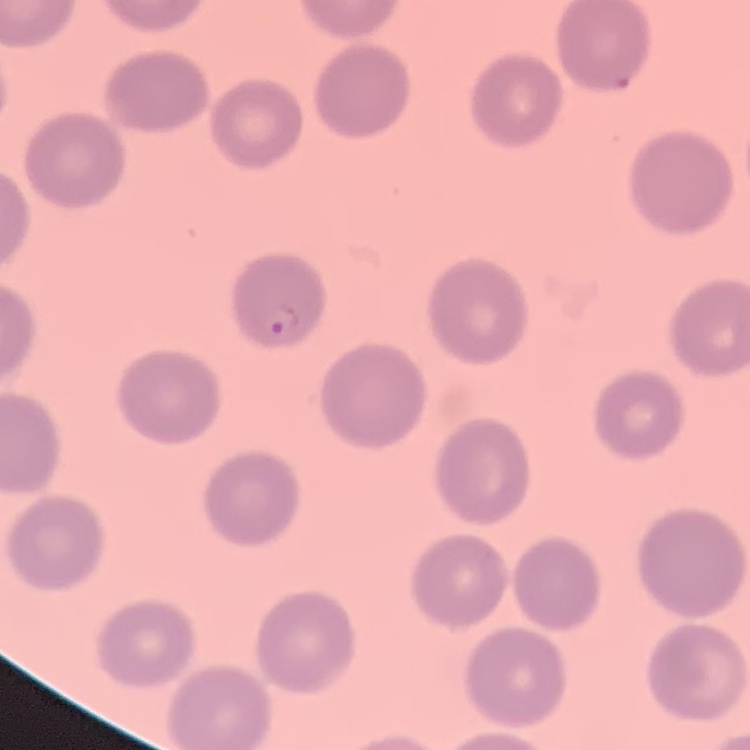 The erythrocytes exhibit no rouleaux formation. Stained with either Field's or Giemsa. One tile cut from a larger photomicrograph. Thin peripheral smear.